Give the location of every white blood cell.
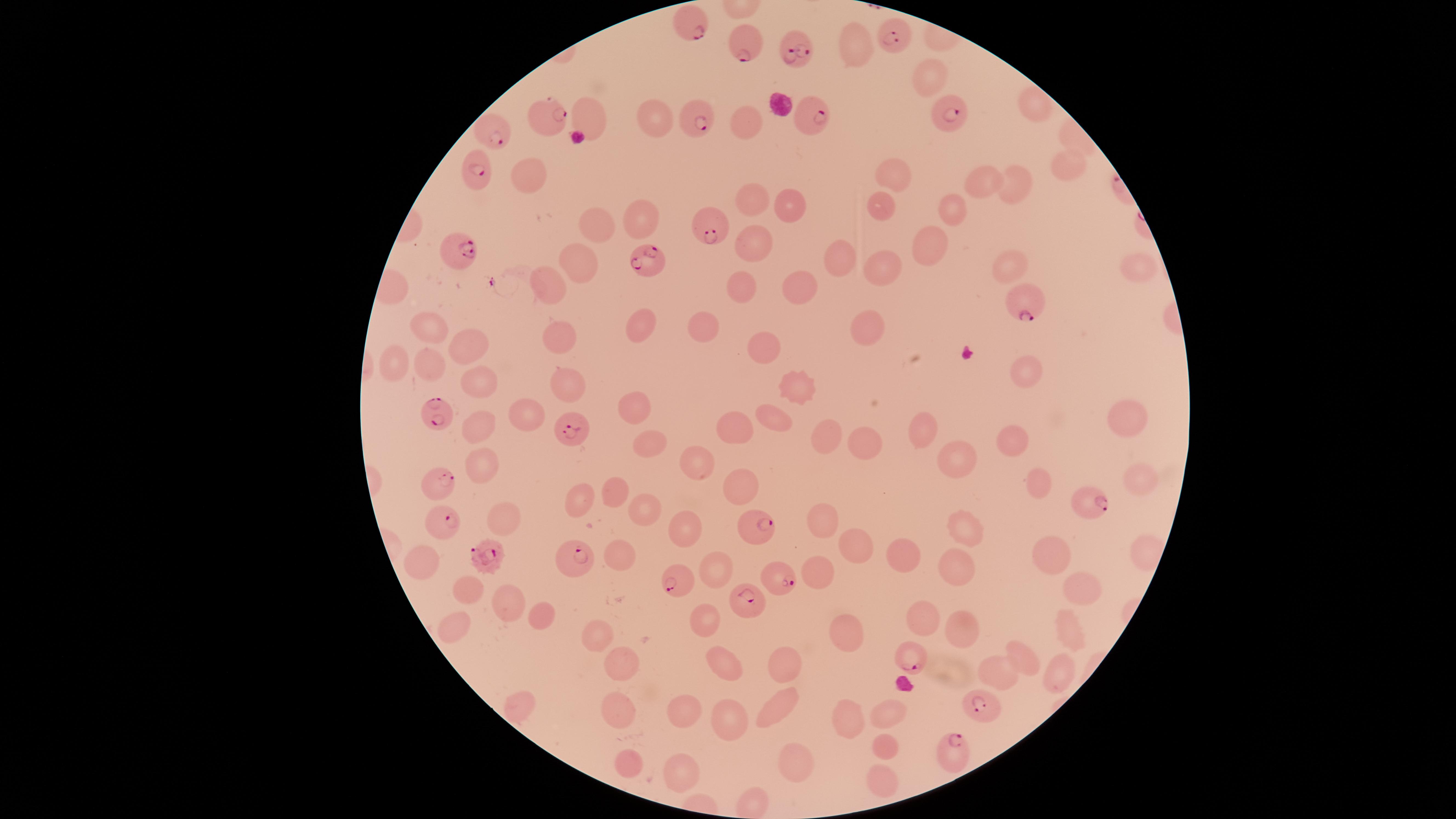

No white blood cells identified.

Approximate marker points as (x, y) in pixels.
Summary:
  - Parasitized red blood cells: (691, 26), (890, 32), (745, 42), (789, 43), (943, 112), (542, 118), (697, 118), (814, 119), (492, 133), (476, 177), (703, 223), (453, 247), (646, 266), (1026, 305), (432, 417), (568, 433), (439, 486), (1085, 503), (440, 514), (761, 530), (486, 555), (579, 559), (781, 581), (675, 583), (753, 601), (909, 658), (983, 712), (954, 752)
  - Uninfected red blood cells: (856, 46), (928, 78), (650, 115), (582, 120), (741, 126), (1066, 163), (528, 174), (893, 174), (978, 181), (1010, 185), (751, 200), (789, 201), (950, 204), (883, 206), (640, 216), (594, 222), (756, 246), (931, 246), (836, 258), (575, 260), (1134, 261), (1008, 265), (881, 267), (553, 278), (739, 281), (799, 281), (634, 326), (703, 326), (427, 327), (866, 331), (558, 336), (472, 340), (764, 348), (390, 365), (429, 367), (1025, 367), (474, 384), (570, 387), (795, 387), (630, 407), (513, 412), (1126, 415), (771, 417), (477, 421), (734, 421), (833, 430), (925, 432), (1009, 438), (859, 444), (646, 446), (955, 446), (479, 463), (700, 465), (1037, 479), (1139, 481), (741, 486), (614, 489), (586, 499), (647, 509), (501, 519), (823, 527), (684, 529), (961, 531), (859, 544), (908, 550), (621, 553), (1049, 553), (419, 564), (954, 564), (817, 570), (720, 573), (463, 591), (1077, 595), (511, 600), (706, 612), (920, 613), (537, 619), (449, 627), (848, 631), (962, 631), (1062, 637), (595, 638), (1023, 651), (622, 661), (784, 663), (727, 664), (1000, 667), (1058, 671), (521, 706), (776, 708), (887, 708), (615, 710), (682, 711), (728, 714), (852, 715), (885, 742), (629, 762), (794, 763), (679, 770), (879, 775)
  - Presence: malaria parasites detected
  - Species: Plasmodium falciparum
  - Preparation: thin blood film
  - Capture: smartphone photograph through the microscope eyepiece
  - Image size: 1456×819 pixels
  - Stain: Giemsa
  - Visible region: circular
  - Field of view: single